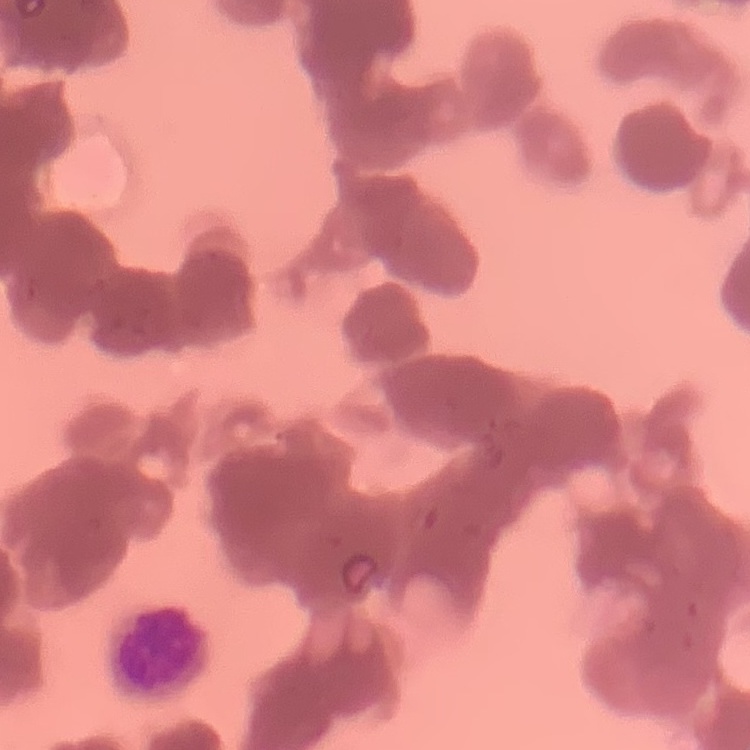

Summary:
  - Erythrocyte morphology: rouleaux formation
  - Image type: one tile cut from a larger photomicrograph
  - Preparation: thin blood smear
  - Stain: Field's or Giemsa